Name the parasite shown.
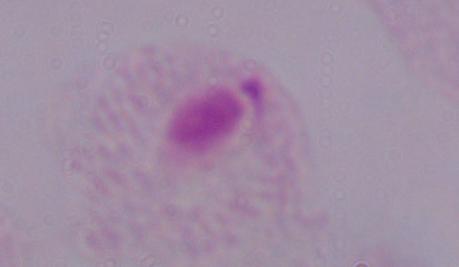
This is a trichomonad.

Summary:
  - Modality: micrograph
  - Magnification: 1000x